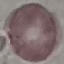

Summary:
  - Malaria status: uninfected
  - Preparation: thin smear
  - Capture: smartphone camera at the microscope eyepiece
  - Image type: automatically extracted cell patch, resized to 64 × 64 pixels
  - Stain: Giemsa